Describe the morphology of the red blood cells.
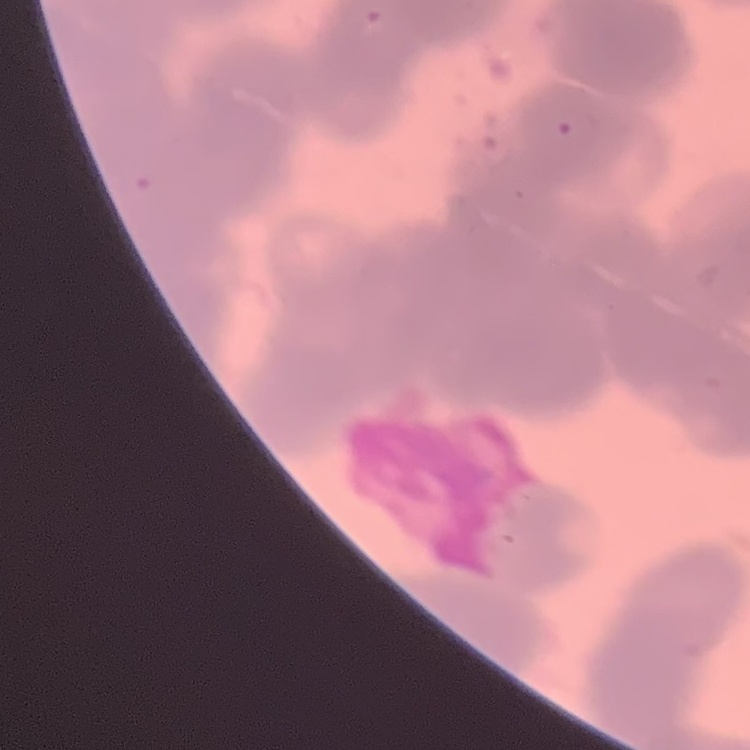
Rouleaux formation.

preparation = thin blood film
image type = square crop of a larger photomicrograph
stain = Field's or Giemsa